Assess the morphology of the erythrocytes.
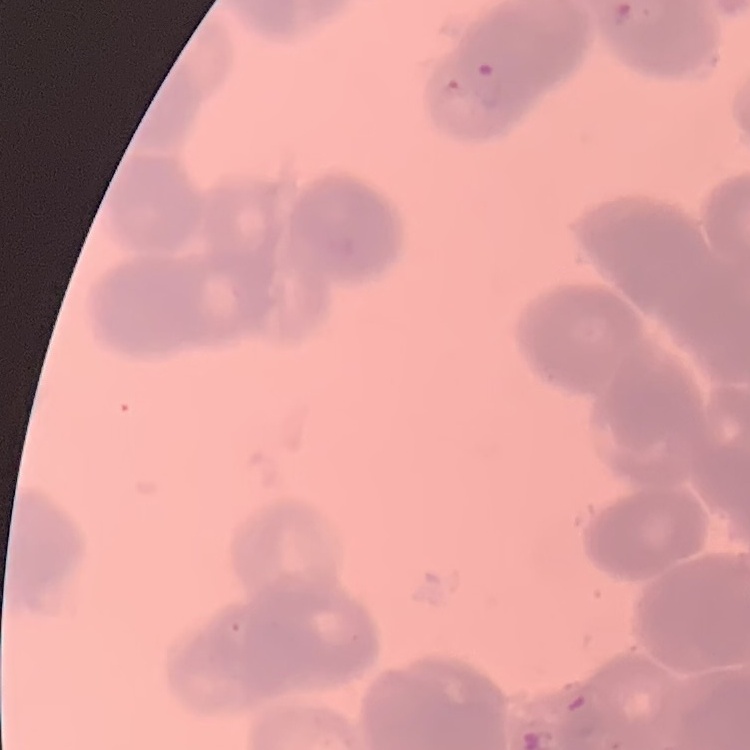

Rouleaux formation.

Stained with either Field's or Giemsa. Thin blood film. One tile cut from a larger photomicrograph.